Name the cell type shown.
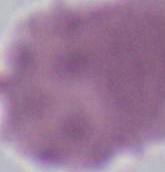

An erythrocyte.

Micrograph. 1000x magnification.